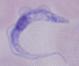

Micrograph. 1000x magnification. A trypanosome is shown.